Give the extent of all Plasmodium falciparum-infected red blood cells.
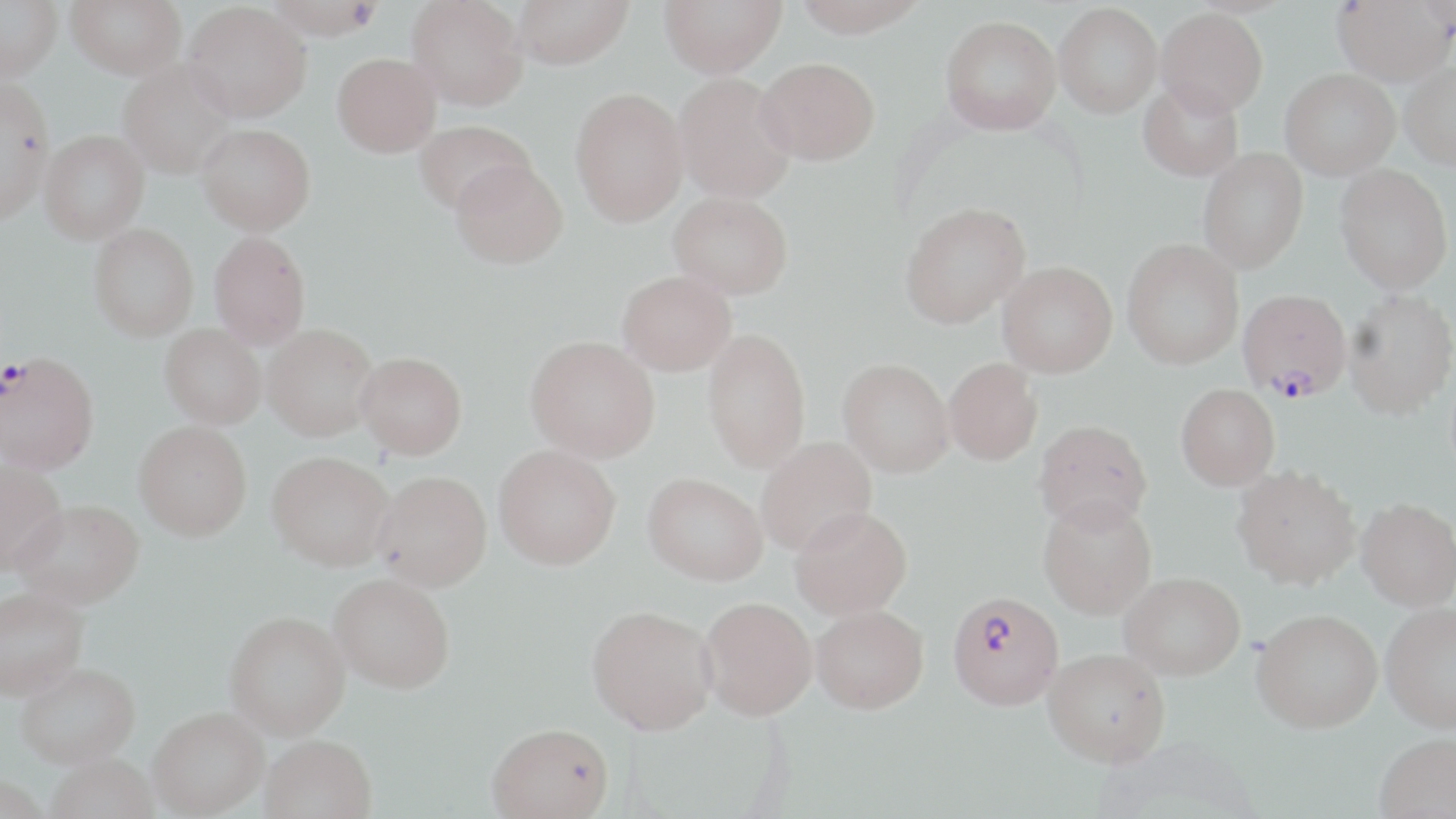

Approximate bounding boxes as (x1,y1)-(x2,y2) corner pairs in pixels.
Plasmodium falciparum-infected red blood cells: (1238,289)-(1352,401), (0,352)-(96,473), (948,591)-(1064,710).

slide-level diagnosis = Plasmodium falciparum
stain = May-Grünwald-Giemsa
modality = light microscopy
magnification = 1000x
uninfected red blood cell locations = approximate bounding boxes as (x1,y1)-(x2,y2) corner pairs in pixels: (0,0)-(62,82), (65,0)-(186,79), (264,0)-(385,39), (406,0)-(528,110), (512,0)-(633,69), (659,0)-(786,76), (793,0)-(928,37), (1332,1)-(1455,85), (183,2)-(312,122), (1054,3)-(1162,117), (1156,8)-(1268,117), (940,15)-(1061,134), (332,53)-(441,157), (755,57)-(879,165), (118,60)-(237,179), (1400,61)-(1456,169), (1280,68)-(1399,179), (673,73)-(797,203), (0,77)-(55,225), (1138,79)-(1244,181), (570,87)-(688,226), (413,120)-(535,215), (197,123)-(316,235), (39,130)-(149,242), (1198,148)-(1308,274), (450,159)-(568,268), (1335,164)-(1453,293), (668,191)-(793,298), (899,202)-(1031,328), (89,223)-(199,341), (209,231)-(311,349), (1122,239)-(1243,370), (997,261)-(1117,377), (617,270)-(736,375), (1344,290)-(1456,419), (262,323)-(379,441), (159,324)-(266,428), (702,328)-(811,472), (525,335)-(659,462), (355,351)-(467,459), (838,358)-(954,477), (944,358)-(1042,465), (1176,383)-(1280,491), (1033,418)-(1152,532), (133,421)-(252,540), (756,437)-(877,557), (494,444)-(621,569), (266,450)-(395,570), (0,460)-(68,574), (1231,464)-(1360,588), (373,470)-(492,591), (643,472)-(767,585), (1038,496)-(1157,618), (1356,497)-(1456,610), (13,499)-(145,608), (790,505)-(912,619), (1119,572)-(1245,680), (329,573)-(455,692), (0,587)-(89,700), (699,596)-(817,720), (1381,603)-(1456,732), (810,604)-(929,713), (587,605)-(717,734), (1251,609)-(1383,733), (225,611)-(350,739), (1043,648)-(1170,766), (15,662)-(140,770), (148,708)-(268,817), (486,722)-(614,818), (1374,733)-(1456,819), (262,734)-(377,819), (46,756)-(160,819), (0,777)-(50,819)
image size = 1456×819 pixels
preparation = thin blood smear
field of view = single